Locate every Plasmodium parasite.
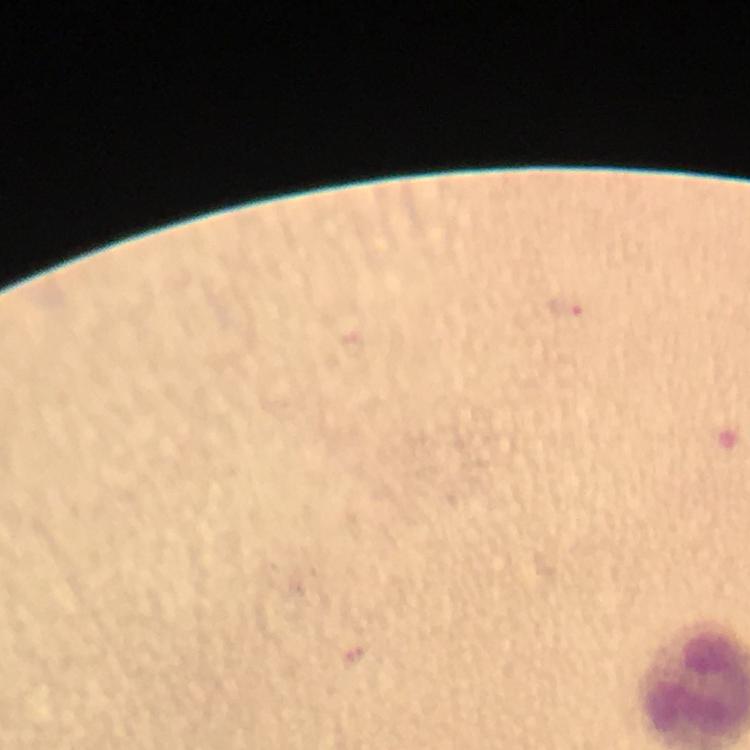
Approximate object centers, in pixels from the top-left corner.
Plasmodium parasites: (x=565, y=306).

Photographed with a smartphone mounted on the microscope. Image is 750×750 pixels. A crop from one field of view. Thick smear. Giemsa stain. 100x magnification. From a malaria diagnostic workup. Immersion oil applied.